Identify the parasite.
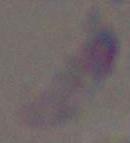

This is Toxoplasma gondii.

Summary:
  - Modality: photomicrograph
  - Magnification: 1000x